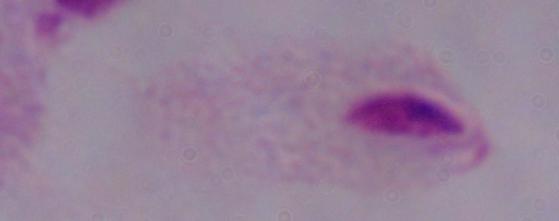

A trichomonad is seen. Captured at 1000x magnification. Photomicrograph.